Locate and identify every blood parasite.
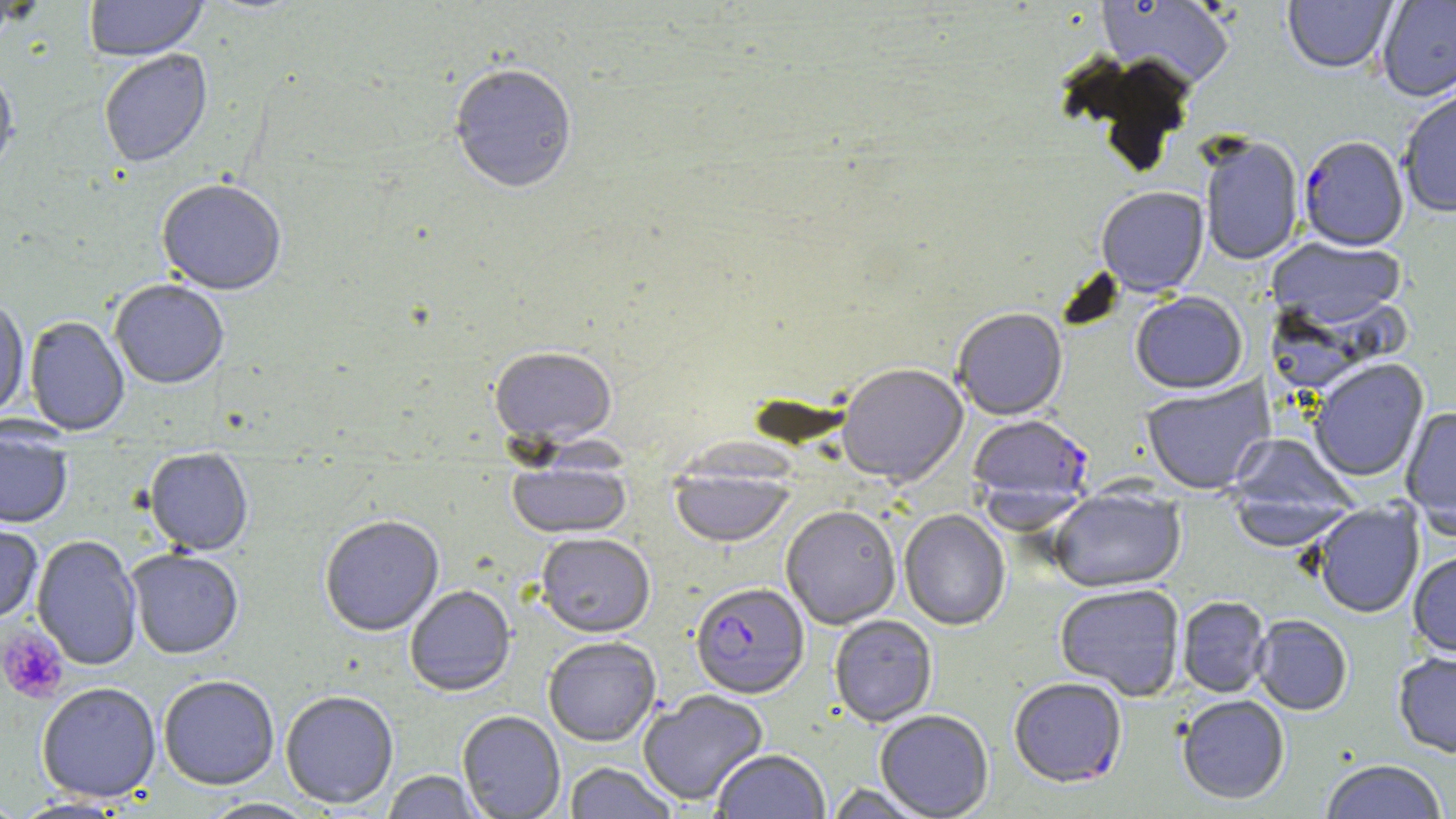

Approximate bounding boxes as (x1,y1)-(x2,y2) corner pairs in pixels.
Plasmodium falciparum-infected red blood cells: (1298,136)-(1409,252), (968,414)-(1095,523), (690,583)-(809,699).
No Plasmodium ovale, Plasmodium malariae, Plasmodium vivax, Babesia divergens, or Trypanosoma brucei observed.

Summary:
  - Uninfected red blood cell locations: (83,0)-(208,62), (1095,0)-(1235,91), (1283,0)-(1398,75), (1376,0)-(1456,102), (98,49)-(213,169), (448,62)-(578,195), (0,64)-(20,181), (1398,87)-(1456,218), (1198,136)-(1304,266), (156,180)-(287,296), (1096,187)-(1209,298), (1266,238)-(1408,333), (109,280)-(229,389), (1131,292)-(1248,395), (1262,296)-(1401,395), (0,298)-(29,420), (952,309)-(1068,421), (24,316)-(130,436), (488,348)-(618,448), (1308,359)-(1429,482), (837,365)-(968,489), (1139,376)-(1274,495), (1401,406)-(1456,538), (0,423)-(73,530), (1226,434)-(1357,528), (143,448)-(254,556), (506,459)-(632,539), (670,463)-(795,548), (1227,490)-(1355,553), (1048,491)-(1186,594), (1311,502)-(1424,619), (781,505)-(901,630), (900,510)-(1011,631), (319,516)-(445,637), (0,520)-(44,625), (535,533)-(656,638), (31,535)-(143,671), (126,548)-(244,660), (1408,552)-(1456,658), (1055,584)-(1185,701), (404,586)-(515,697), (1177,596)-(1272,698), (1251,615)-(1352,716), (829,616)-(938,727), (543,637)-(661,747), (1393,651)-(1456,759), (158,675)-(279,791), (1008,678)-(1127,790), (37,683)-(161,803), (280,690)-(399,810), (638,690)-(769,806), (1176,696)-(1290,805), (457,711)-(565,819), (875,711)-(994,818), (712,750)-(830,819), (1320,760)-(1448,819), (564,763)-(679,818), (381,771)-(485,818), (823,783)-(933,818), (0,795)-(30,818), (13,797)-(131,818), (200,798)-(320,819)
  - Platelet locations: (0,625)-(68,704)
  - Slide-level diagnosis: Plasmodium falciparum
  - Preparation: thin blood film
  - Stain: May-Grünwald-Giemsa
  - Image size: 1456×819 pixels
  - Modality: optical microscopy
  - Field of view: single
  - Magnification: 1000x